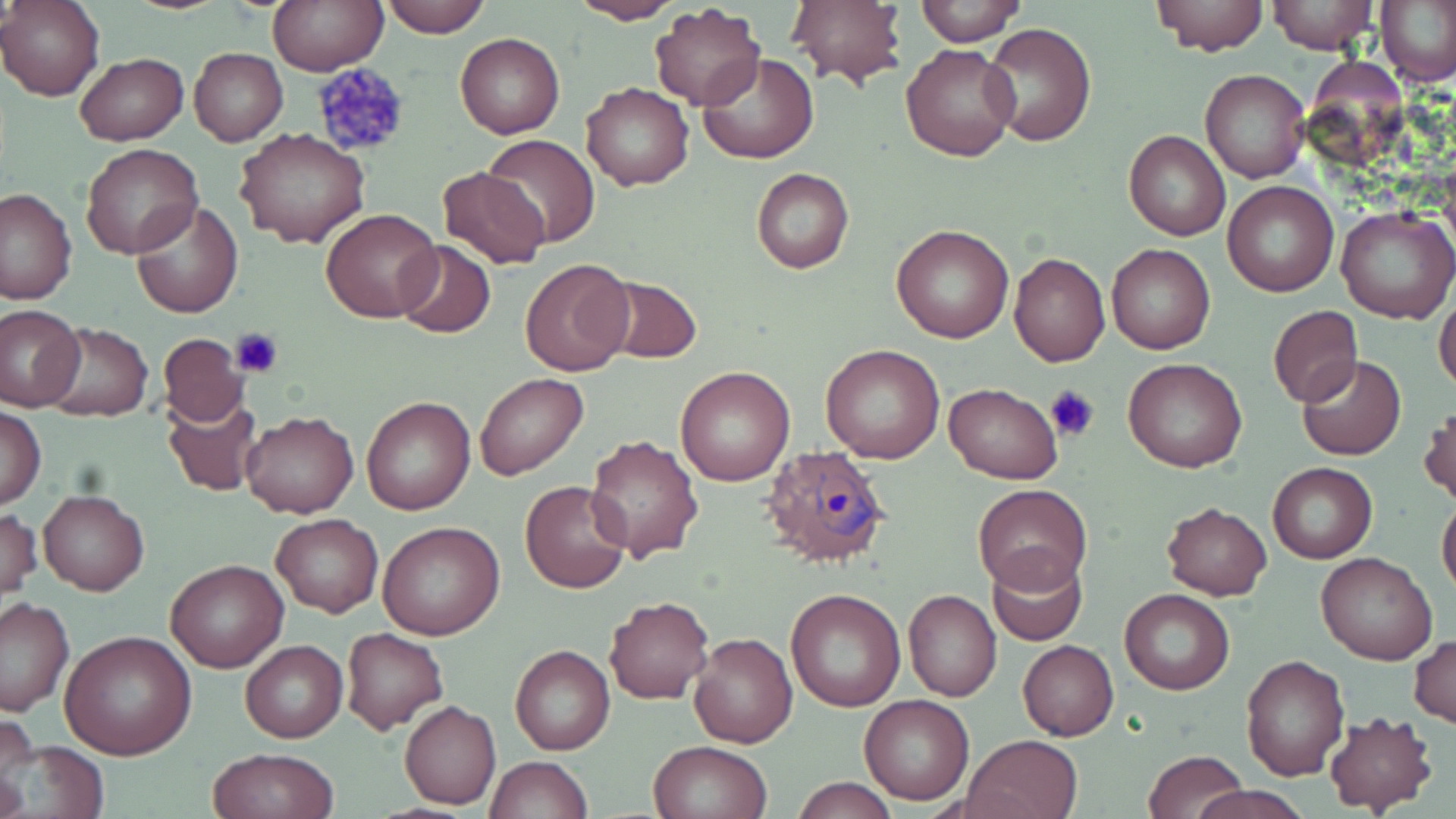
Approximate bounding boxes as (x1,y1)-(x2,y2) corner pairs in pixels. Uninfected red blood cell locations: (1,0)-(104,102), (268,0)-(386,74), (377,0)-(489,37), (786,0)-(907,90), (911,0)-(1026,46), (1152,0)-(1268,56), (1266,0)-(1380,55), (1377,0)-(1456,89), (567,1)-(687,25), (649,4)-(766,111), (983,23)-(1095,146), (456,32)-(565,139), (900,43)-(1019,163), (189,48)-(289,146), (75,52)-(188,147), (698,53)-(819,164), (1200,69)-(1310,183), (581,81)-(694,191), (237,128)-(368,248), (1123,130)-(1231,241), (482,134)-(601,248), (80,143)-(203,260), (436,167)-(553,271), (750,169)-(855,275), (1222,180)-(1339,298), (1,188)-(76,305), (131,199)-(245,319), (1336,205)-(1455,323), (321,207)-(441,322), (891,223)-(1014,343), (393,241)-(496,339), (1106,243)-(1216,354), (1009,251)-(1110,366), (519,255)-(636,376), (600,275)-(702,365), (1434,292)-(1456,397), (1,306)-(84,412), (1268,306)-(1362,407), (41,322)-(152,421), (155,333)-(248,427), (820,345)-(945,464), (1295,355)-(1407,459), (1123,357)-(1249,474), (675,364)-(795,486), (475,373)-(588,480), (944,383)-(1064,483), (361,395)-(476,516), (162,396)-(263,497), (1420,404)-(1455,509), (1,405)-(45,510), (239,410)-(359,519), (583,434)-(704,562), (1267,462)-(1377,564), (520,480)-(633,595), (972,484)-(1092,592), (38,488)-(150,596), (1437,495)-(1456,600), (1160,501)-(1273,600), (1,508)-(41,603), (271,513)-(383,618), (378,521)-(505,641), (985,546)-(1088,644), (1315,550)-(1437,665), (165,559)-(288,671), (785,589)-(906,711), (1119,589)-(1234,694), (903,590)-(1002,702), (0,596)-(74,717), (604,596)-(714,705), (342,628)-(448,735), (61,630)-(198,759), (688,633)-(797,747), (1412,634)-(1455,728), (241,640)-(347,742), (1017,640)-(1119,740), (509,644)-(615,755), (1240,654)-(1350,782), (859,694)-(975,805), (400,699)-(501,810), (1322,710)-(1437,814), (963,734)-(1082,819), (2,740)-(110,819), (650,740)-(771,819), (210,749)-(338,819), (1142,749)-(1248,819), (484,755)-(594,818), (793,778)-(898,818), (1191,784)-(1312,819). Platelet locations: (309,65)-(412,159), (231,325)-(285,377), (1045,384)-(1101,445). Plasmodium ovale-infected red blood cell locations: (762,444)-(894,574). Slide-level diagnosis: Plasmodium ovale. Light microscopy. Single field of view. Thin blood film. May-Grünwald-Giemsa stain. Captured at 1000x magnification. Image is 1456×819 pixels.